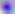

Summary:
  - Identification: Toxoplasma gondii
  - Magnification: 400x
  - Modality: micrograph